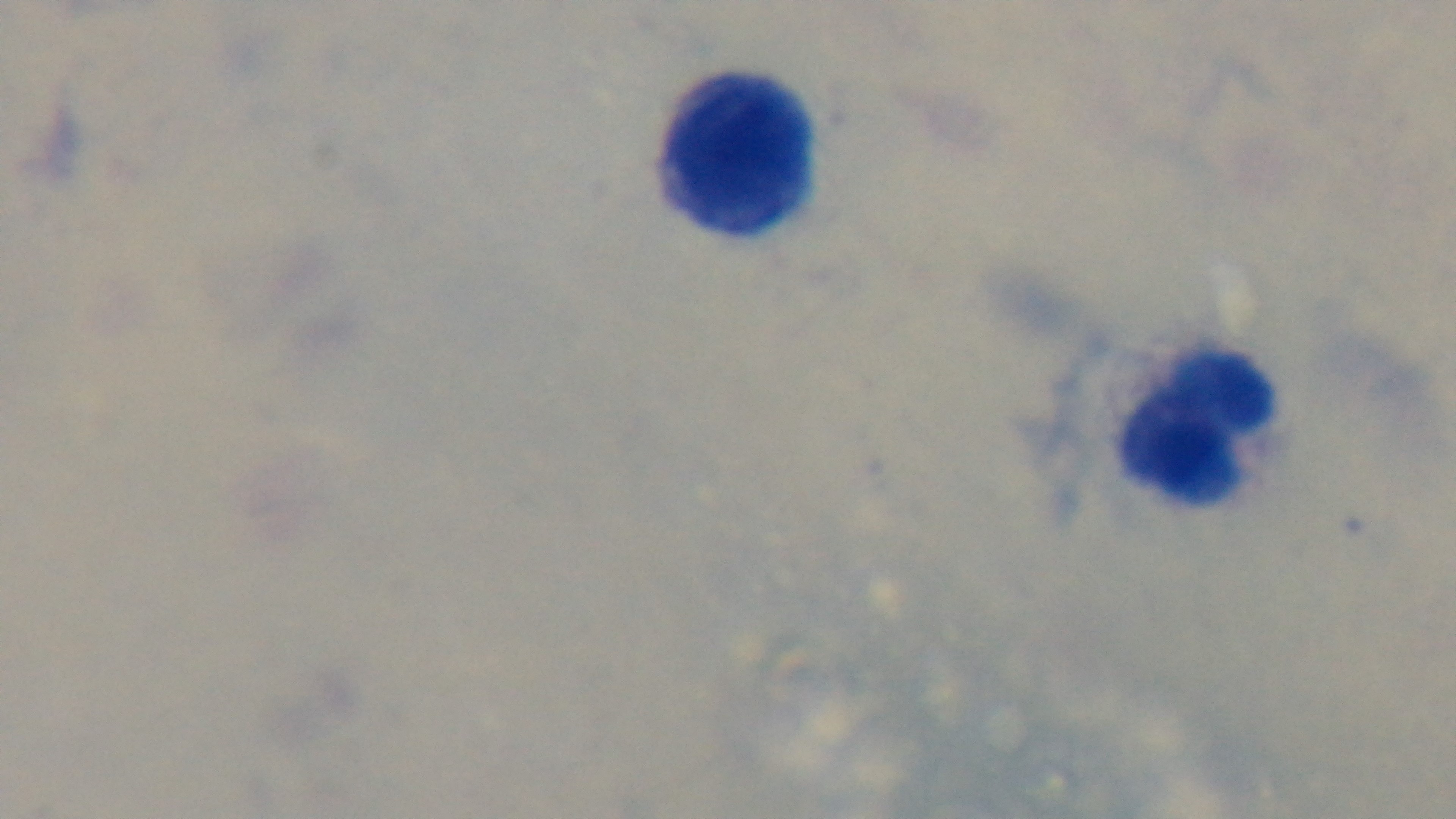 Light microscopy. Captured with a mounted 4K digital camera. Malaria status: negative. One field from the slide. Giemsa stain. Preparation: thick. Oil-immersion objective, 100x.